Classify this cell by malaria status.
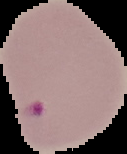

Parasitized.

Cell region segmented out of the field of view; the surrounding area is masked to black. Image is 127×154 pixels. From a thin blood smear.